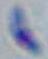 1000x magnification. Micrograph. Toxoplasma gondii is seen.